Give the position of every malaria parasite.
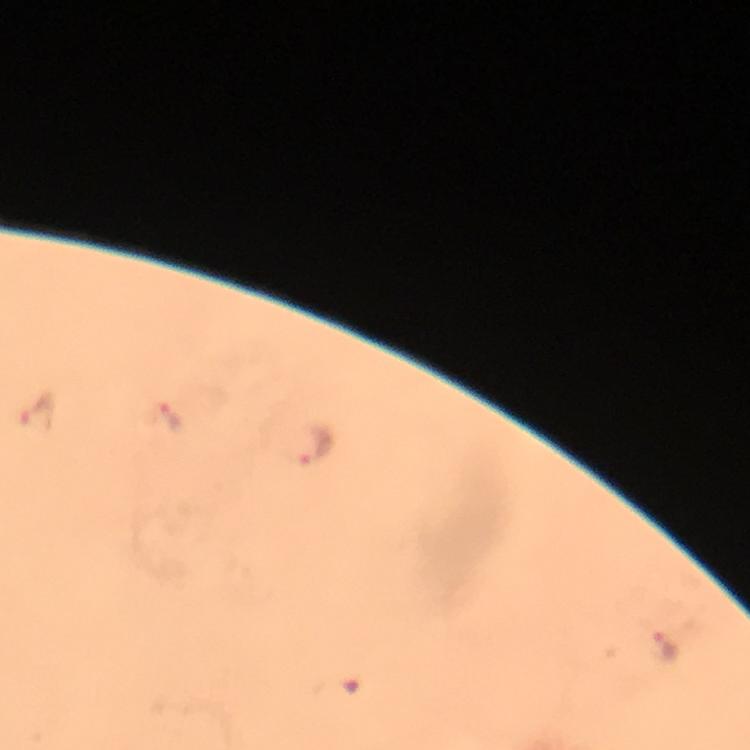
Approximate centers as (x, y) in pixels.
Malaria parasites: (37, 410), (170, 418), (315, 444), (669, 651).

Summary:
  - Cropped from: a single field of view
  - Preparation: thick smear
  - Image size: 750×750 pixels
  - Context: from a malaria diagnostic workup
  - Immersion oil: used
  - Stain: Giemsa
  - Capture: smartphone camera through the microscope
  - Magnification: 100x